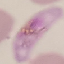

Summary:
  - Malaria status: parasitized
  - Capture: smartphone camera at the microscope eyepiece
  - Stain: Giemsa
  - Image type: cell patch, automatically extracted from a larger field of view and resized to 64 × 64 pixels
  - Preparation: thin blood film